Assess this cell for malaria.
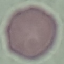

It is uninfected.

Photographed with a smartphone camera at the microscope eyepiece. Automatically extracted cell patch, resized to 64 × 64 pixels. Giemsa-stained preparation. Thin smear of blood.